Assess this cell for malaria.
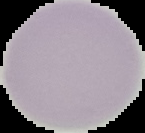
It is uninfected.

Segmented cell region on a black background. From a thin blood film. Image is 145×133 pixels.